Identify the cell.
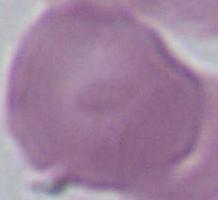
An erythrocyte.

magnification = 1000x
modality = micrograph